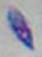 Toxoplasma gondii is seen. 1000x magnification. Photomicrograph.